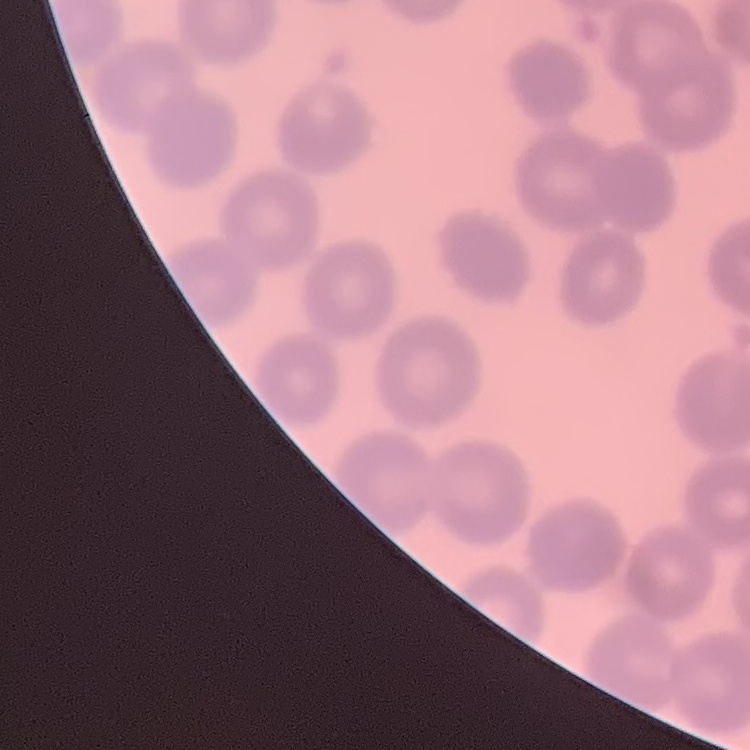

red blood cell morphology = no rouleaux formation
preparation = thin peripheral smear
stain = Field's or Giemsa
image type = square crop of a larger photomicrograph